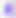

modality = micrograph
magnification = 400x
identification = Toxoplasma gondii